Assess this cell for malaria.
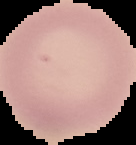
It is uninfected.

The area outside the segmented cell region is set to black. Image is 136×145 pixels. From a thin blood film.